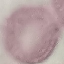

malaria status = uninfected
capture = smartphone camera at the microscope eyepiece
image type = automatically extracted cell patch, resized to 64 × 64 pixels
stain = Giemsa
preparation = thin smear